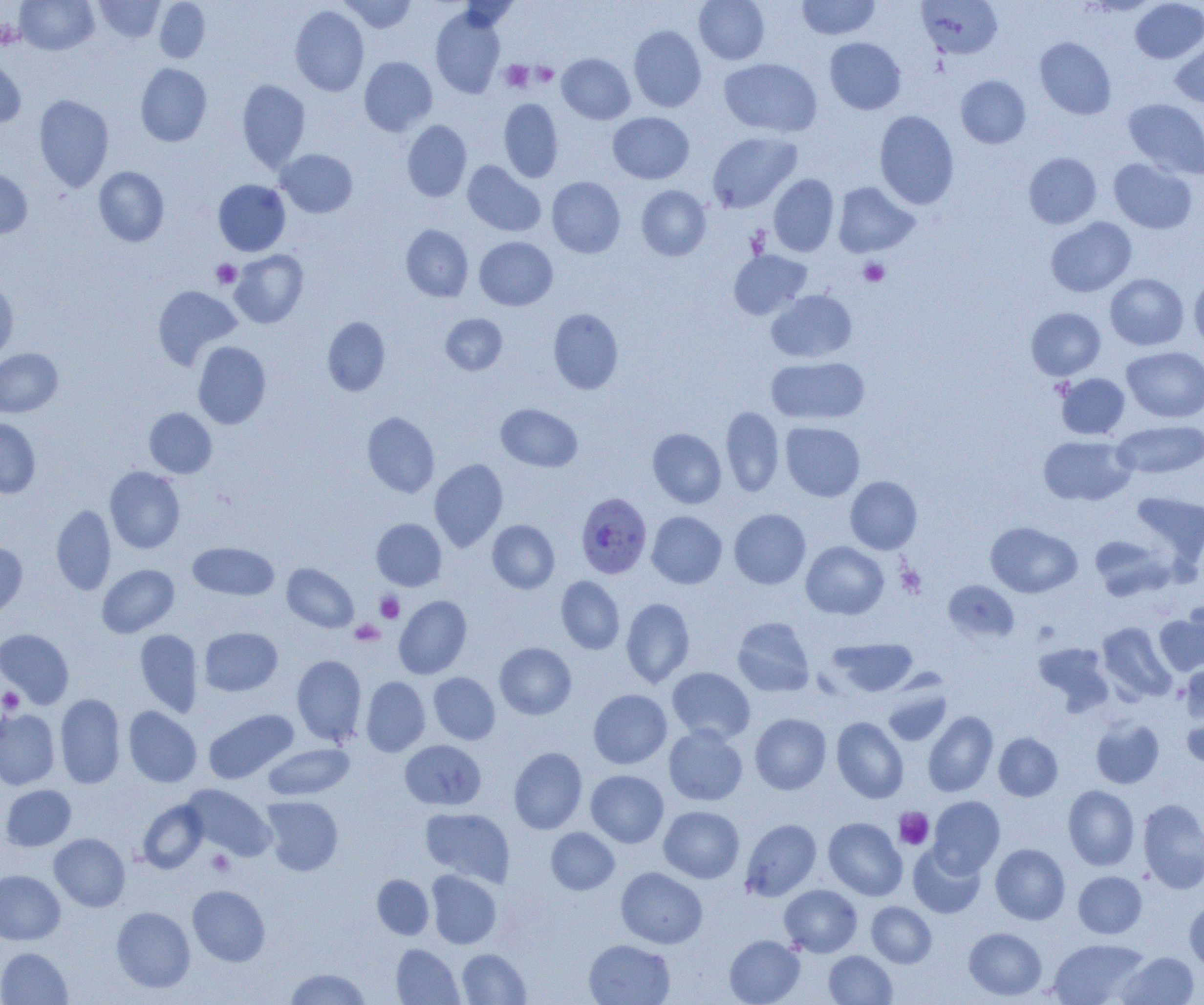

Summary:
  - Coordinate format: approximate bounding boxes as [x1, y1, x2, y2] in pixels
  - Platelet locations: [0, 20, 23, 49], [501, 60, 534, 91], [532, 63, 558, 86], [859, 258, 889, 286], [211, 259, 241, 288], [896, 565, 926, 598], [376, 592, 404, 623], [350, 620, 384, 646], [1, 688, 24, 712], [894, 807, 934, 849], [206, 849, 235, 876]
  - Uninfected red blood cell locations: [16, 0, 98, 55], [94, 0, 164, 43], [154, 0, 210, 62], [339, 0, 416, 33], [694, 0, 769, 64], [916, 0, 1002, 59], [1130, 0, 1204, 63], [796, 1, 880, 40], [290, 5, 369, 96], [431, 8, 506, 98], [628, 25, 707, 112], [825, 37, 905, 114], [1035, 37, 1116, 119], [1170, 39, 1204, 109], [0, 53, 26, 128], [557, 53, 635, 124], [359, 56, 438, 136], [719, 58, 822, 138], [135, 63, 212, 146], [955, 75, 1030, 148], [237, 79, 310, 171], [34, 94, 114, 192], [499, 98, 563, 183], [1123, 99, 1204, 179], [874, 110, 959, 210], [608, 112, 694, 184], [402, 120, 471, 202], [707, 131, 802, 213], [277, 149, 357, 218], [1023, 152, 1102, 229], [1109, 158, 1197, 234], [462, 161, 545, 237], [94, 166, 169, 246], [0, 168, 32, 239], [769, 174, 839, 256], [547, 176, 625, 257], [213, 180, 290, 256], [833, 182, 918, 257], [636, 185, 711, 260], [1046, 217, 1136, 297], [401, 225, 473, 301], [474, 236, 557, 310], [229, 250, 308, 328], [728, 250, 812, 320], [1105, 273, 1188, 350], [1189, 275, 1204, 353], [0, 278, 18, 363], [152, 285, 242, 370], [766, 290, 857, 363], [1026, 307, 1105, 380], [548, 308, 624, 394], [440, 313, 508, 375], [322, 316, 390, 396], [193, 341, 271, 429], [1122, 347, 1204, 423], [0, 348, 62, 417], [766, 356, 870, 424], [1056, 373, 1130, 439], [496, 403, 582, 471], [721, 406, 784, 497], [144, 408, 216, 478], [362, 412, 440, 497], [0, 418, 41, 498], [780, 421, 865, 501], [1113, 421, 1204, 479], [648, 428, 726, 508], [1038, 435, 1135, 505], [429, 459, 508, 551], [105, 467, 185, 553], [845, 476, 922, 554], [1130, 492, 1204, 569], [52, 503, 116, 595], [729, 508, 810, 589], [647, 511, 727, 588], [371, 518, 446, 591], [487, 520, 559, 593], [985, 521, 1082, 598], [1089, 535, 1171, 600], [0, 541, 27, 616], [801, 541, 889, 619], [188, 542, 279, 600], [97, 564, 179, 637], [282, 564, 358, 633], [556, 576, 625, 654], [944, 580, 1019, 642], [394, 595, 472, 678], [621, 597, 695, 688], [1183, 598, 1204, 668], [1154, 611, 1204, 674], [732, 617, 815, 697], [1097, 622, 1177, 703], [199, 626, 282, 696], [0, 628, 74, 708], [135, 629, 203, 717], [828, 637, 918, 696], [495, 642, 576, 719], [1033, 642, 1114, 714], [291, 655, 366, 746], [1181, 662, 1204, 724], [667, 667, 755, 744], [428, 672, 500, 745], [360, 676, 430, 757], [882, 685, 952, 746], [588, 689, 672, 768], [55, 693, 125, 788], [1181, 702, 1204, 772], [123, 706, 202, 787], [0, 709, 59, 790], [204, 709, 298, 783], [923, 711, 998, 797], [750, 713, 831, 794], [831, 717, 909, 803], [1090, 717, 1164, 788], [664, 726, 747, 806], [993, 732, 1063, 801], [400, 739, 486, 810], [263, 743, 354, 799], [509, 747, 587, 834], [586, 770, 668, 847], [1, 784, 76, 851], [183, 784, 276, 860], [1063, 785, 1139, 870], [928, 795, 1005, 877], [260, 796, 343, 875], [138, 799, 208, 873], [1138, 799, 1204, 893], [659, 805, 744, 883], [420, 807, 515, 886], [823, 817, 907, 900], [740, 819, 821, 901], [546, 827, 619, 895], [49, 833, 130, 911], [908, 843, 986, 918], [990, 843, 1070, 924], [616, 867, 707, 948], [0, 869, 65, 944], [426, 870, 501, 949], [1073, 871, 1147, 938], [372, 874, 434, 939], [779, 884, 862, 957], [187, 885, 270, 966], [1184, 899, 1204, 974], [867, 902, 936, 968], [111, 906, 195, 992], [964, 927, 1047, 1000], [724, 935, 805, 1005], [1048, 938, 1149, 1005], [584, 939, 675, 1005], [391, 944, 464, 1004], [0, 947, 72, 1004], [457, 948, 531, 1004], [824, 950, 897, 1005], [1117, 951, 1199, 1005], [284, 968, 371, 1004]
  - Plasmodium falciparum-infected red blood cell locations: [576, 493, 652, 578]
  - Slide-level diagnosis: Plasmodium falciparum
  - Modality: light microscopy
  - Magnification: 1000x
  - Preparation: thin blood smear
  - Field of view: single
  - Image size: 1204×1005 pixels